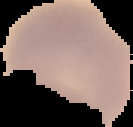
Summary:
  - Result: negative for malaria parasites
  - Preparation: thin blood film
  - Image type: segmented cell region on a black background
  - Image size: 133×127 pixels